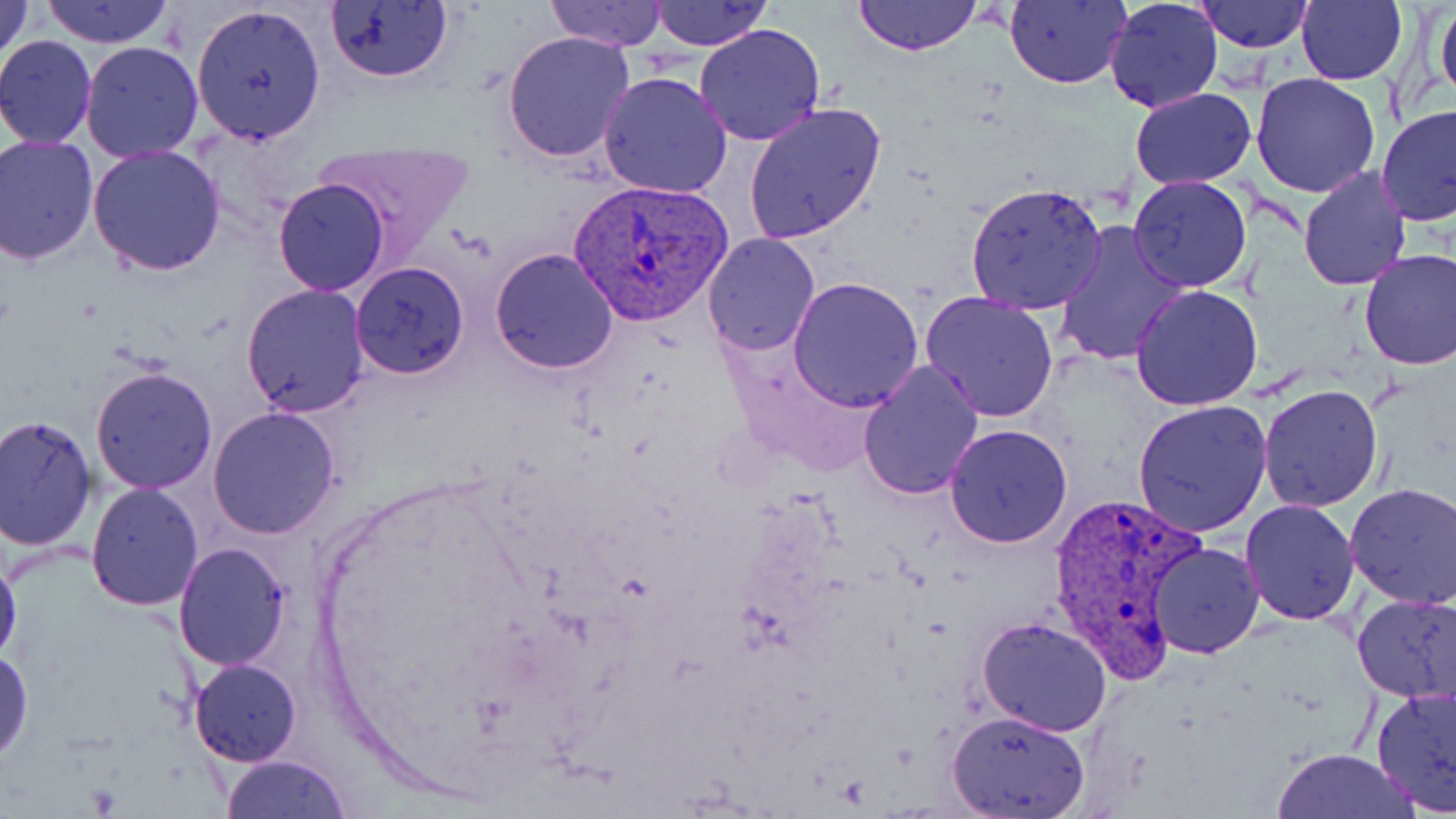

Summary:
  - Coordinate format: approximate bounding boxes as (x1,y1)-(x2,y2) corner pairs in pixels
  - Uninfected red blood cell locations: (41,0)-(174,47), (324,0)-(453,84), (546,0)-(666,49), (647,0)-(772,51), (854,0)-(981,55), (1004,0)-(1131,88), (1102,0)-(1223,115), (1193,0)-(1314,52), (1297,0)-(1407,86), (1430,0)-(1455,113), (0,1)-(35,62), (190,2)-(327,143), (694,23)-(826,147), (501,30)-(635,163), (0,35)-(99,147), (79,42)-(204,163), (599,70)-(733,197), (1251,72)-(1381,197), (1131,89)-(1257,190), (743,100)-(886,244), (1377,106)-(1456,229), (0,134)-(99,265), (312,141)-(474,255), (86,146)-(227,278), (1298,166)-(1412,291), (1128,176)-(1253,292), (273,177)-(389,296), (965,181)-(1109,314), (1052,221)-(1194,368), (700,232)-(820,356), (489,247)-(620,373), (1358,249)-(1456,370), (349,260)-(469,380), (788,275)-(924,411), (241,283)-(370,418), (1130,285)-(1263,410), (919,293)-(1061,426), (857,359)-(984,501), (90,367)-(218,494), (1257,386)-(1384,512), (1132,401)-(1275,539), (209,407)-(341,539), (0,414)-(97,551), (944,425)-(1072,548), (85,482)-(204,611), (1344,484)-(1456,608), (1240,499)-(1359,625), (1147,541)-(1265,658), (173,543)-(292,670), (0,547)-(22,670), (1351,593)-(1456,703), (978,615)-(1111,736), (0,648)-(33,763), (189,658)-(302,764), (1370,685)-(1456,813), (946,709)-(1092,818), (1270,749)-(1419,819), (221,754)-(352,818)
  - Plasmodium vivax-infected red blood cell locations: (566,178)-(734,325), (1046,489)-(1206,679)
  - Slide-level diagnosis: Plasmodium vivax
  - Image size: 1456×819 pixels
  - Preparation: thin blood smear
  - Stain: May-Grünwald-Giemsa
  - Field of view: one of a larger specimen
  - Modality: optical microscopy
  - Magnification: 1000x